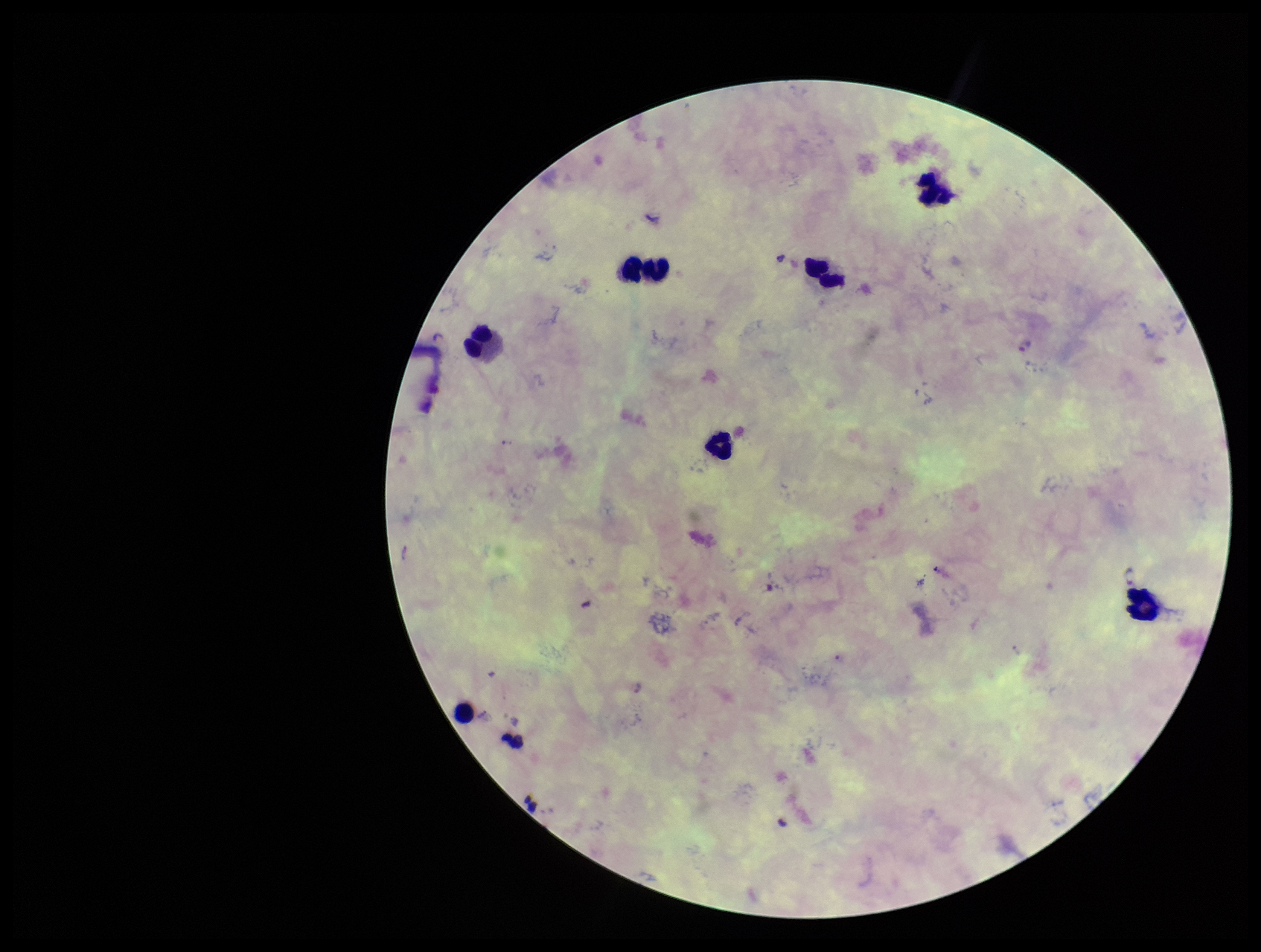
Summary:
  - Parasite count: 2
  - Plasmodium parasites: detected
  - Stain: Giemsa
  - Image size: 1261×952 pixels
  - Field of view: one from this slide
  - Species reported for this patient: Plasmodium falciparum
  - Preparation: thick
  - Leukocyte count: 7
  - Patient malaria status: positive
  - Capture: smartphone photograph through the microscope eyepiece